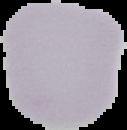
Summary:
  - Result: negative for Plasmodium parasites
  - Preparation: thin blood film
  - Image size: 127×130 pixels
  - Image type: segmented cell region with the area outside set to black